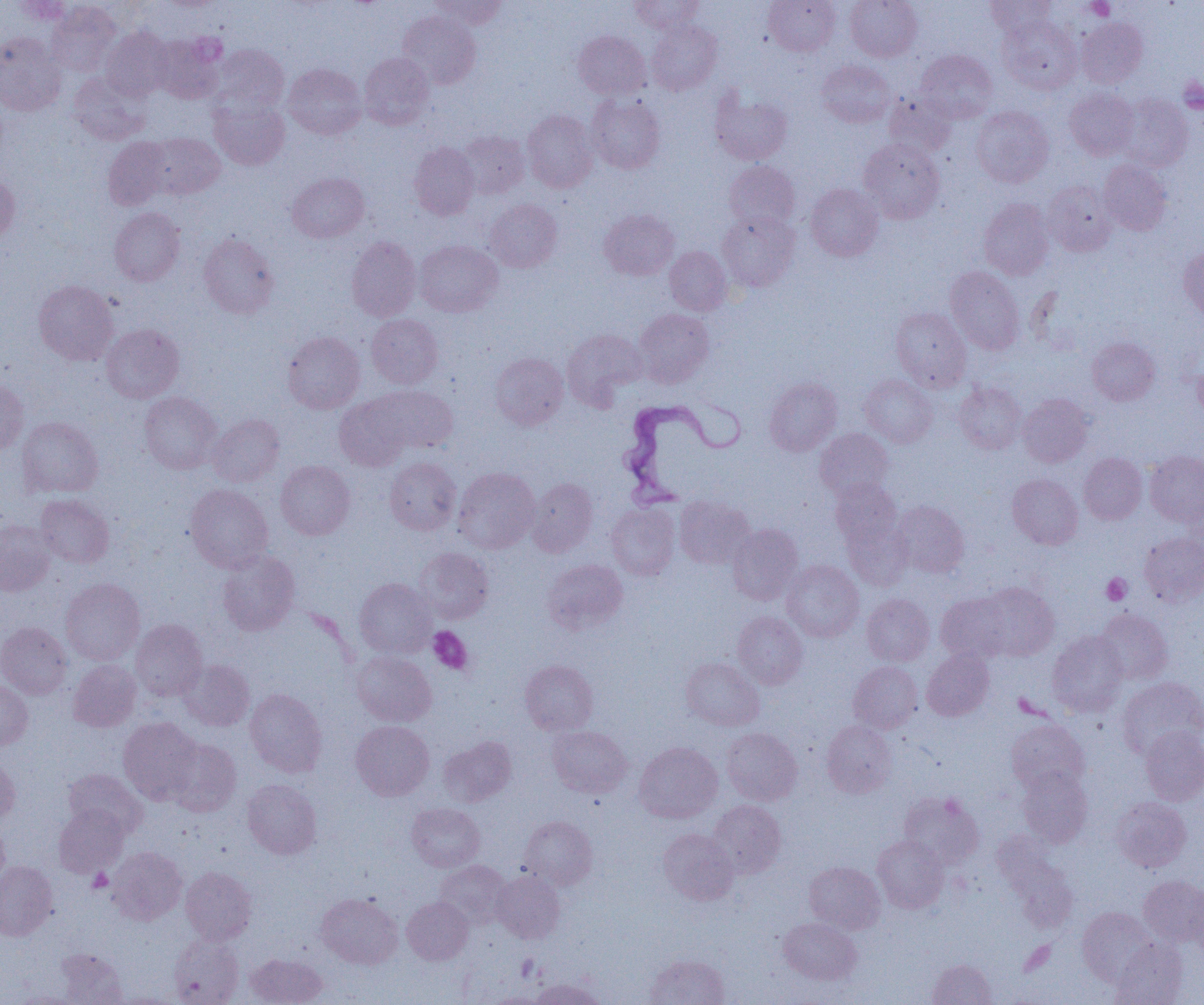

slide-level diagnosis = Trypanosoma brucei
magnification = 1000x
field of view = one of a larger specimen
image size = 1204×1005 pixels
platelet locations = approximate bounding boxes as named x1/y1/x2/y2 corners in pixels: (x1=1086, y1=0, x2=1114, y2=20), (x1=1178, y1=76, x2=1204, y2=113), (x1=1101, y1=573, x2=1131, y2=605), (x1=428, y1=626, x2=473, y2=675), (x1=87, y1=868, x2=113, y2=892), (x1=516, y1=954, x2=540, y2=982)
Trypanosoma brucei locations = approximate bounding boxes as named x1/y1/x2/y2 corners in pixels: (x1=616, y1=396, x2=744, y2=507)
uninfected red blood cell locations = approximate bounding boxes as named x1/y1/x2/y2 corners in pixels: (x1=429, y1=0, x2=507, y2=29), (x1=628, y1=0, x2=704, y2=33), (x1=764, y1=0, x2=840, y2=56), (x1=845, y1=0, x2=922, y2=61), (x1=985, y1=0, x2=1055, y2=38), (x1=10, y1=1, x2=73, y2=25), (x1=47, y1=2, x2=121, y2=76), (x1=397, y1=11, x2=481, y2=89), (x1=998, y1=16, x2=1082, y2=94), (x1=1076, y1=17, x2=1148, y2=87), (x1=647, y1=21, x2=721, y2=95), (x1=101, y1=26, x2=171, y2=101), (x1=573, y1=30, x2=650, y2=99), (x1=0, y1=32, x2=65, y2=116), (x1=151, y1=35, x2=223, y2=103), (x1=212, y1=44, x2=289, y2=115), (x1=915, y1=50, x2=997, y2=123), (x1=359, y1=52, x2=434, y2=129), (x1=816, y1=60, x2=896, y2=127), (x1=283, y1=63, x2=367, y2=139), (x1=69, y1=73, x2=150, y2=145), (x1=1065, y1=87, x2=1139, y2=159), (x1=710, y1=89, x2=792, y2=165), (x1=884, y1=92, x2=956, y2=157), (x1=586, y1=94, x2=666, y2=173), (x1=1118, y1=94, x2=1193, y2=171), (x1=210, y1=98, x2=289, y2=170), (x1=971, y1=105, x2=1054, y2=187), (x1=522, y1=109, x2=598, y2=193), (x1=457, y1=130, x2=530, y2=199), (x1=144, y1=132, x2=225, y2=199), (x1=102, y1=137, x2=172, y2=210), (x1=859, y1=138, x2=945, y2=223), (x1=409, y1=142, x2=479, y2=219), (x1=1098, y1=160, x2=1171, y2=236), (x1=724, y1=161, x2=800, y2=231), (x1=0, y1=172, x2=20, y2=246), (x1=287, y1=172, x2=369, y2=242), (x1=1043, y1=181, x2=1117, y2=256), (x1=806, y1=183, x2=883, y2=261), (x1=979, y1=198, x2=1054, y2=279), (x1=484, y1=199, x2=563, y2=272), (x1=109, y1=207, x2=185, y2=286), (x1=599, y1=208, x2=679, y2=280), (x1=717, y1=211, x2=799, y2=291), (x1=199, y1=232, x2=279, y2=319), (x1=346, y1=236, x2=421, y2=321), (x1=415, y1=240, x2=502, y2=317), (x1=665, y1=246, x2=731, y2=315), (x1=1179, y1=246, x2=1204, y2=320), (x1=945, y1=266, x2=1024, y2=354), (x1=33, y1=279, x2=118, y2=365), (x1=890, y1=307, x2=971, y2=391), (x1=634, y1=308, x2=714, y2=387), (x1=366, y1=314, x2=443, y2=388), (x1=101, y1=323, x2=184, y2=402), (x1=562, y1=329, x2=647, y2=409), (x1=282, y1=332, x2=365, y2=413), (x1=1087, y1=337, x2=1160, y2=405), (x1=490, y1=352, x2=568, y2=429), (x1=1194, y1=359, x2=1204, y2=420), (x1=860, y1=375, x2=937, y2=448), (x1=0, y1=377, x2=29, y2=454), (x1=763, y1=377, x2=842, y2=456), (x1=954, y1=382, x2=1026, y2=454), (x1=368, y1=385, x2=458, y2=454), (x1=139, y1=392, x2=222, y2=474), (x1=1017, y1=393, x2=1093, y2=467), (x1=334, y1=396, x2=411, y2=470), (x1=208, y1=415, x2=284, y2=486), (x1=17, y1=416, x2=103, y2=497), (x1=815, y1=428, x2=894, y2=500), (x1=1145, y1=451, x2=1204, y2=527), (x1=1079, y1=453, x2=1147, y2=524), (x1=385, y1=457, x2=461, y2=534), (x1=276, y1=460, x2=355, y2=540), (x1=453, y1=467, x2=540, y2=553), (x1=1007, y1=474, x2=1083, y2=549), (x1=527, y1=478, x2=598, y2=557), (x1=830, y1=478, x2=902, y2=550), (x1=185, y1=484, x2=273, y2=572), (x1=35, y1=494, x2=114, y2=568), (x1=1182, y1=495, x2=1203, y2=557), (x1=675, y1=497, x2=755, y2=569), (x1=891, y1=501, x2=969, y2=578), (x1=607, y1=503, x2=680, y2=580), (x1=841, y1=516, x2=913, y2=590), (x1=0, y1=518, x2=55, y2=596), (x1=728, y1=524, x2=804, y2=604), (x1=1139, y1=532, x2=1204, y2=606), (x1=414, y1=548, x2=494, y2=623), (x1=217, y1=550, x2=300, y2=636), (x1=541, y1=559, x2=627, y2=635), (x1=782, y1=560, x2=864, y2=642), (x1=61, y1=578, x2=144, y2=665), (x1=354, y1=578, x2=436, y2=658), (x1=977, y1=582, x2=1059, y2=661), (x1=862, y1=593, x2=934, y2=666), (x1=936, y1=593, x2=1012, y2=664), (x1=1095, y1=609, x2=1173, y2=685), (x1=732, y1=611, x2=807, y2=689), (x1=131, y1=619, x2=207, y2=700), (x1=0, y1=622, x2=71, y2=699), (x1=1047, y1=632, x2=1128, y2=716), (x1=922, y1=650, x2=994, y2=720), (x1=352, y1=651, x2=436, y2=726), (x1=681, y1=657, x2=764, y2=730), (x1=178, y1=659, x2=255, y2=731), (x1=68, y1=660, x2=141, y2=732), (x1=520, y1=660, x2=598, y2=735), (x1=848, y1=661, x2=923, y2=733), (x1=1117, y1=677, x2=1204, y2=759), (x1=0, y1=680, x2=33, y2=749), (x1=245, y1=689, x2=326, y2=776), (x1=119, y1=717, x2=202, y2=804), (x1=1006, y1=719, x2=1089, y2=795), (x1=350, y1=720, x2=435, y2=800), (x1=821, y1=720, x2=896, y2=798), (x1=548, y1=726, x2=632, y2=798), (x1=1139, y1=726, x2=1204, y2=805), (x1=721, y1=727, x2=802, y2=805), (x1=438, y1=736, x2=516, y2=806), (x1=165, y1=737, x2=240, y2=815), (x1=634, y1=742, x2=722, y2=823), (x1=0, y1=757, x2=20, y2=826), (x1=1017, y1=767, x2=1093, y2=848), (x1=63, y1=769, x2=147, y2=837), (x1=242, y1=779, x2=322, y2=859), (x1=899, y1=791, x2=984, y2=869), (x1=1111, y1=797, x2=1192, y2=872), (x1=707, y1=800, x2=786, y2=878), (x1=406, y1=803, x2=484, y2=872), (x1=54, y1=805, x2=129, y2=877), (x1=519, y1=816, x2=598, y2=889), (x1=0, y1=820, x2=9, y2=889), (x1=659, y1=828, x2=738, y2=904), (x1=872, y1=835, x2=949, y2=913), (x1=999, y1=844, x2=1078, y2=932), (x1=106, y1=847, x2=187, y2=925), (x1=435, y1=860, x2=512, y2=927), (x1=0, y1=861, x2=57, y2=940), (x1=804, y1=861, x2=885, y2=934), (x1=180, y1=866, x2=257, y2=944), (x1=492, y1=870, x2=564, y2=944), (x1=1139, y1=875, x2=1204, y2=947), (x1=1188, y1=883, x2=1204, y2=961), (x1=316, y1=892, x2=403, y2=968), (x1=402, y1=896, x2=473, y2=964), (x1=1077, y1=907, x2=1157, y2=985), (x1=778, y1=917, x2=862, y2=984), (x1=169, y1=936, x2=244, y2=1005), (x1=1111, y1=938, x2=1188, y2=1005), (x1=55, y1=948, x2=127, y2=1004), (x1=245, y1=953, x2=328, y2=1005), (x1=647, y1=954, x2=729, y2=1005), (x1=928, y1=958, x2=996, y2=1005), (x1=531, y1=978, x2=605, y2=1005), (x1=12, y1=991, x2=88, y2=1004), (x1=488, y1=992, x2=547, y2=1004)
modality = light microscopy
preparation = thin blood smear